Mark where platelets are.
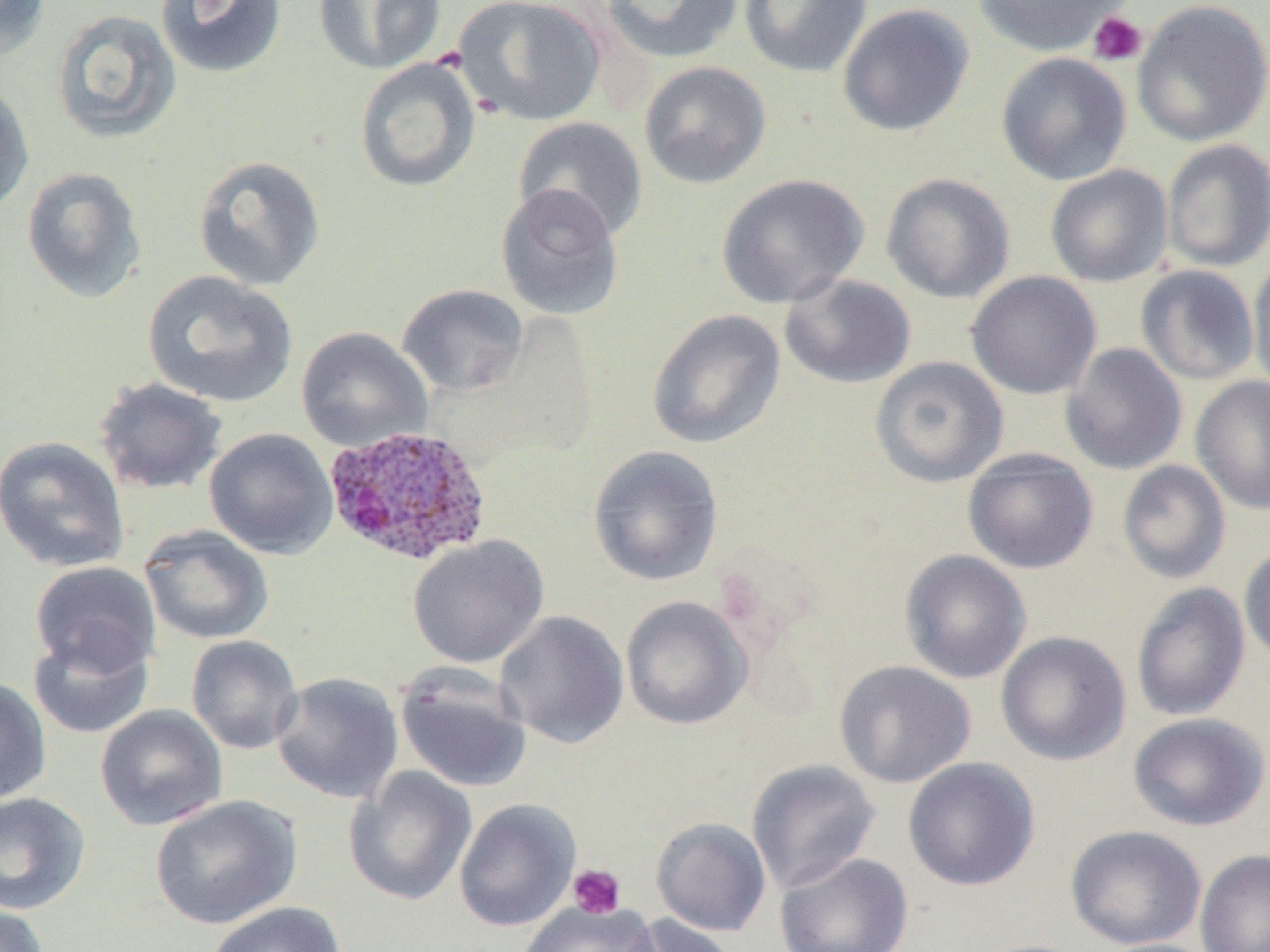
Approximate bounding boxes as named x1/y1/x2/y2 corners in pixels.
Platelets: (x1=1087, y1=11, x2=1147, y2=66), (x1=568, y1=865, x2=625, y2=919).

plasmodium_ovale_infected_red_blood_cell_locations: 'approximate bounding boxes as named x1/y1/x2/y2 corners in pixels: (x1=322, y1=424, x2=492, y2=567)'
slide_level_diagnosis: Plasmodium ovale
preparation: thin blood film
magnification: 1000x
stain: May-Grünwald-Giemsa
field_of_view: one of a larger specimen
uninfected_red_blood_cell_locations: 'approximate bounding boxes as named x1/y1/x2/y2 corners in pixels: (x1=0, y1=0, x2=51, y2=62), (x1=155, y1=0, x2=287, y2=80), (x1=313, y1=0, x2=445, y2=74), (x1=453, y1=0, x2=607, y2=126), (x1=600, y1=0, x2=743, y2=64), (x1=738, y1=0, x2=872, y2=78), (x1=972, y1=0, x2=1133, y2=57), (x1=1132, y1=1, x2=1270, y2=148), (x1=837, y1=4, x2=975, y2=137), (x1=51, y1=8, x2=182, y2=145), (x1=996, y1=52, x2=1132, y2=186), (x1=354, y1=56, x2=481, y2=193), (x1=639, y1=61, x2=771, y2=189), (x1=0, y1=78, x2=34, y2=220), (x1=513, y1=116, x2=649, y2=241), (x1=1162, y1=139, x2=1270, y2=273), (x1=192, y1=154, x2=326, y2=292), (x1=1045, y1=164, x2=1173, y2=287), (x1=21, y1=166, x2=147, y2=304), (x1=881, y1=172, x2=1015, y2=304), (x1=716, y1=173, x2=869, y2=309), (x1=495, y1=184, x2=625, y2=322), (x1=1247, y1=256, x2=1270, y2=400), (x1=1136, y1=264, x2=1259, y2=386), (x1=141, y1=270, x2=299, y2=409), (x1=966, y1=271, x2=1101, y2=399), (x1=779, y1=273, x2=917, y2=389), (x1=397, y1=283, x2=530, y2=397), (x1=646, y1=309, x2=786, y2=449), (x1=296, y1=327, x2=432, y2=453), (x1=1060, y1=342, x2=1187, y2=475), (x1=870, y1=356, x2=1009, y2=488), (x1=1190, y1=375, x2=1270, y2=515), (x1=93, y1=376, x2=228, y2=495), (x1=204, y1=427, x2=339, y2=560), (x1=0, y1=435, x2=131, y2=573), (x1=587, y1=445, x2=724, y2=587), (x1=963, y1=449, x2=1099, y2=574), (x1=1117, y1=460, x2=1231, y2=584), (x1=139, y1=524, x2=275, y2=645), (x1=407, y1=534, x2=550, y2=668), (x1=1239, y1=542, x2=1270, y2=665), (x1=899, y1=549, x2=1032, y2=684), (x1=29, y1=561, x2=161, y2=678), (x1=1131, y1=582, x2=1250, y2=722), (x1=620, y1=596, x2=753, y2=730), (x1=494, y1=610, x2=629, y2=748), (x1=27, y1=630, x2=155, y2=739), (x1=996, y1=631, x2=1131, y2=766), (x1=186, y1=635, x2=303, y2=754), (x1=834, y1=660, x2=976, y2=789), (x1=395, y1=663, x2=533, y2=794), (x1=271, y1=672, x2=404, y2=804), (x1=0, y1=677, x2=52, y2=806), (x1=95, y1=704, x2=228, y2=831), (x1=1127, y1=712, x2=1269, y2=831), (x1=902, y1=756, x2=1040, y2=890), (x1=746, y1=758, x2=881, y2=894), (x1=344, y1=765, x2=477, y2=907), (x1=0, y1=792, x2=90, y2=915), (x1=150, y1=795, x2=302, y2=930), (x1=454, y1=798, x2=581, y2=932), (x1=651, y1=817, x2=772, y2=937), (x1=1065, y1=825, x2=1207, y2=950), (x1=1195, y1=849, x2=1270, y2=952), (x1=774, y1=852, x2=914, y2=952), (x1=518, y1=901, x2=660, y2=952), (x1=206, y1=902, x2=346, y2=952), (x1=0, y1=903, x2=49, y2=952), (x1=623, y1=914, x2=739, y2=952), (x1=1094, y1=938, x2=1219, y2=952)'
modality: optical microscopy
image_size: 1270×952 pixels